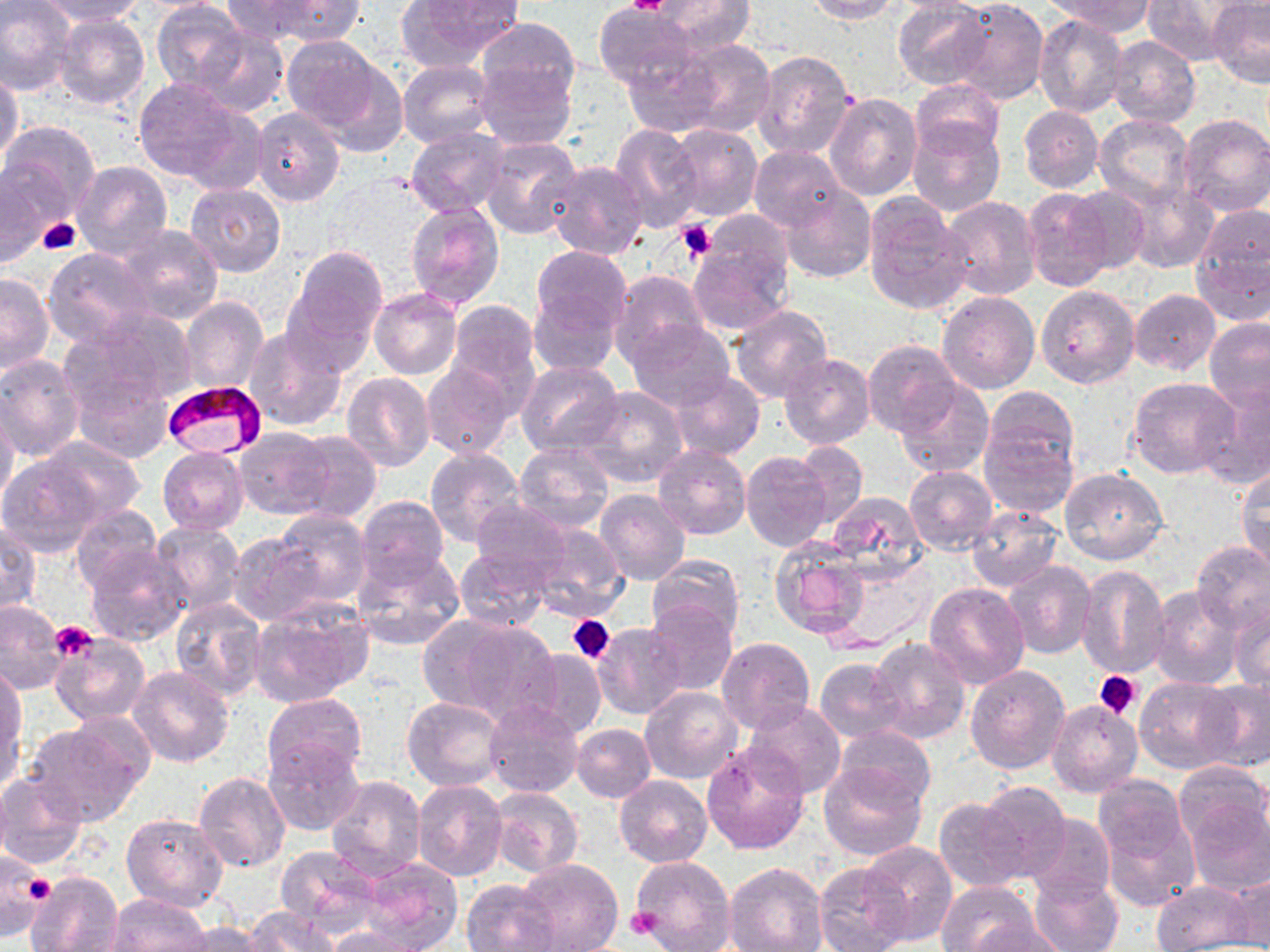

Summary:
  - Coordinate format: approximate bounding boxes as named x1/y1/x2/y2 corners in pixels
  - Plasmodium falciparum-infected red blood cell locations: (x1=162, y1=379, x2=268, y2=456)
  - Platelet locations: (x1=626, y1=0, x2=673, y2=16), (x1=38, y1=217, x2=82, y2=253), (x1=676, y1=220, x2=718, y2=262), (x1=568, y1=614, x2=615, y2=664), (x1=52, y1=624, x2=96, y2=660), (x1=1095, y1=670, x2=1141, y2=719), (x1=12, y1=866, x2=55, y2=920), (x1=626, y1=906, x2=664, y2=940)
  - Uninfected red blood cell locations: (x1=1, y1=0, x2=78, y2=96), (x1=32, y1=0, x2=148, y2=24), (x1=222, y1=0, x2=318, y2=41), (x1=254, y1=0, x2=367, y2=45), (x1=650, y1=0, x2=754, y2=56), (x1=804, y1=0, x2=899, y2=24), (x1=892, y1=0, x2=991, y2=89), (x1=949, y1=0, x2=1047, y2=105), (x1=1049, y1=0, x2=1155, y2=35), (x1=1142, y1=0, x2=1244, y2=66), (x1=1207, y1=0, x2=1270, y2=88), (x1=396, y1=1, x2=521, y2=69), (x1=152, y1=2, x2=247, y2=93), (x1=594, y1=3, x2=698, y2=93), (x1=51, y1=11, x2=150, y2=111), (x1=1034, y1=15, x2=1128, y2=118), (x1=476, y1=17, x2=582, y2=114), (x1=194, y1=27, x2=288, y2=117), (x1=281, y1=36, x2=386, y2=135), (x1=1107, y1=36, x2=1200, y2=127), (x1=679, y1=38, x2=777, y2=139), (x1=621, y1=45, x2=724, y2=136), (x1=753, y1=50, x2=857, y2=158), (x1=307, y1=51, x2=411, y2=158), (x1=476, y1=58, x2=575, y2=150), (x1=398, y1=60, x2=496, y2=149), (x1=0, y1=70, x2=22, y2=168), (x1=133, y1=76, x2=253, y2=185), (x1=912, y1=79, x2=1004, y2=158), (x1=825, y1=93, x2=922, y2=200), (x1=1018, y1=104, x2=1103, y2=194), (x1=252, y1=109, x2=344, y2=206), (x1=1178, y1=113, x2=1270, y2=218), (x1=1094, y1=114, x2=1195, y2=209), (x1=907, y1=119, x2=1004, y2=217), (x1=1, y1=120, x2=100, y2=221), (x1=668, y1=123, x2=761, y2=222), (x1=609, y1=124, x2=703, y2=233), (x1=405, y1=127, x2=510, y2=217), (x1=480, y1=135, x2=582, y2=240), (x1=748, y1=146, x2=847, y2=232), (x1=72, y1=161, x2=172, y2=260), (x1=546, y1=161, x2=648, y2=261), (x1=0, y1=163, x2=59, y2=265), (x1=185, y1=182, x2=285, y2=277), (x1=1068, y1=184, x2=1151, y2=272), (x1=1125, y1=184, x2=1218, y2=274), (x1=782, y1=186, x2=875, y2=282), (x1=1022, y1=187, x2=1114, y2=292), (x1=814, y1=193, x2=916, y2=296), (x1=863, y1=194, x2=971, y2=315), (x1=939, y1=195, x2=1041, y2=301), (x1=404, y1=201, x2=505, y2=311), (x1=1189, y1=208, x2=1269, y2=321), (x1=698, y1=212, x2=796, y2=297), (x1=113, y1=223, x2=223, y2=324), (x1=687, y1=244, x2=792, y2=336), (x1=533, y1=245, x2=631, y2=333), (x1=287, y1=246, x2=387, y2=349), (x1=43, y1=248, x2=158, y2=351), (x1=0, y1=272, x2=53, y2=376), (x1=609, y1=272, x2=710, y2=369), (x1=1036, y1=286, x2=1139, y2=389), (x1=370, y1=288, x2=462, y2=380), (x1=528, y1=288, x2=619, y2=375), (x1=1129, y1=289, x2=1220, y2=374), (x1=937, y1=291, x2=1039, y2=394), (x1=178, y1=295, x2=269, y2=396), (x1=445, y1=300, x2=541, y2=405), (x1=729, y1=305, x2=835, y2=406), (x1=77, y1=306, x2=199, y2=406), (x1=1204, y1=316, x2=1270, y2=411), (x1=629, y1=320, x2=736, y2=410), (x1=243, y1=325, x2=348, y2=431), (x1=862, y1=339, x2=962, y2=435), (x1=778, y1=352, x2=876, y2=449), (x1=0, y1=355, x2=85, y2=463), (x1=421, y1=360, x2=517, y2=462), (x1=514, y1=360, x2=622, y2=456), (x1=71, y1=369, x2=174, y2=464), (x1=342, y1=372, x2=435, y2=471), (x1=667, y1=372, x2=765, y2=459), (x1=894, y1=376, x2=994, y2=477), (x1=1127, y1=378, x2=1239, y2=479), (x1=1196, y1=382, x2=1270, y2=488), (x1=982, y1=386, x2=1079, y2=481), (x1=576, y1=387, x2=687, y2=489), (x1=0, y1=404, x2=20, y2=510), (x1=978, y1=420, x2=1077, y2=520), (x1=234, y1=427, x2=335, y2=519), (x1=289, y1=429, x2=381, y2=522), (x1=41, y1=437, x2=144, y2=521), (x1=792, y1=439, x2=868, y2=526), (x1=515, y1=443, x2=615, y2=531), (x1=653, y1=445, x2=751, y2=540), (x1=158, y1=446, x2=247, y2=534), (x1=425, y1=448, x2=524, y2=548), (x1=741, y1=451, x2=833, y2=551), (x1=0, y1=453, x2=103, y2=557), (x1=1237, y1=464, x2=1270, y2=572), (x1=904, y1=466, x2=997, y2=555), (x1=1059, y1=467, x2=1170, y2=567), (x1=594, y1=488, x2=690, y2=585), (x1=826, y1=491, x2=929, y2=583), (x1=356, y1=495, x2=451, y2=584), (x1=470, y1=497, x2=572, y2=580), (x1=965, y1=504, x2=1063, y2=592), (x1=69, y1=506, x2=163, y2=594), (x1=272, y1=510, x2=371, y2=607), (x1=526, y1=521, x2=628, y2=619), (x1=1, y1=522, x2=41, y2=615), (x1=150, y1=522, x2=245, y2=615), (x1=227, y1=533, x2=325, y2=626), (x1=768, y1=536, x2=871, y2=638), (x1=82, y1=542, x2=191, y2=647), (x1=1191, y1=542, x2=1270, y2=638), (x1=351, y1=546, x2=464, y2=652), (x1=456, y1=548, x2=551, y2=632), (x1=647, y1=554, x2=745, y2=644), (x1=1004, y1=560, x2=1097, y2=659), (x1=821, y1=562, x2=939, y2=656), (x1=1075, y1=565, x2=1170, y2=679), (x1=925, y1=582, x2=1030, y2=690), (x1=1148, y1=586, x2=1242, y2=689), (x1=1230, y1=596, x2=1269, y2=693), (x1=169, y1=597, x2=267, y2=701), (x1=1, y1=601, x2=66, y2=692), (x1=249, y1=602, x2=373, y2=704), (x1=646, y1=602, x2=738, y2=693), (x1=443, y1=619, x2=564, y2=726), (x1=593, y1=623, x2=688, y2=720), (x1=52, y1=633, x2=149, y2=725), (x1=866, y1=636, x2=970, y2=744), (x1=717, y1=638, x2=814, y2=734), (x1=520, y1=649, x2=607, y2=739), (x1=458, y1=656, x2=579, y2=771), (x1=814, y1=657, x2=909, y2=744), (x1=1, y1=662, x2=26, y2=775), (x1=965, y1=664, x2=1072, y2=774), (x1=129, y1=666, x2=235, y2=768), (x1=1134, y1=676, x2=1239, y2=773), (x1=1197, y1=677, x2=1270, y2=772), (x1=754, y1=683, x2=914, y2=791), (x1=640, y1=686, x2=743, y2=785), (x1=261, y1=692, x2=368, y2=783), (x1=402, y1=695, x2=506, y2=790), (x1=483, y1=698, x2=584, y2=799), (x1=1046, y1=700, x2=1144, y2=798), (x1=743, y1=702, x2=847, y2=798), (x1=27, y1=718, x2=148, y2=826), (x1=572, y1=724, x2=656, y2=803), (x1=833, y1=726, x2=936, y2=807), (x1=263, y1=737, x2=364, y2=836), (x1=702, y1=744, x2=808, y2=854), (x1=1173, y1=764, x2=1269, y2=846), (x1=819, y1=765, x2=928, y2=862), (x1=0, y1=770, x2=88, y2=870), (x1=194, y1=771, x2=290, y2=872), (x1=615, y1=775, x2=712, y2=867), (x1=324, y1=776, x2=426, y2=881), (x1=974, y1=779, x2=1074, y2=880), (x1=412, y1=780, x2=509, y2=881), (x1=488, y1=786, x2=583, y2=879), (x1=1093, y1=786, x2=1201, y2=914), (x1=1184, y1=795, x2=1269, y2=894), (x1=933, y1=797, x2=1030, y2=893), (x1=122, y1=812, x2=228, y2=912), (x1=1023, y1=812, x2=1115, y2=900), (x1=860, y1=842, x2=956, y2=946), (x1=275, y1=845, x2=382, y2=932), (x1=0, y1=852, x2=54, y2=939), (x1=630, y1=855, x2=737, y2=952), (x1=353, y1=858, x2=465, y2=952), (x1=514, y1=858, x2=623, y2=952), (x1=725, y1=861, x2=827, y2=952), (x1=814, y1=862, x2=910, y2=952), (x1=1226, y1=869, x2=1270, y2=950), (x1=25, y1=870, x2=123, y2=952), (x1=1028, y1=874, x2=1123, y2=952), (x1=462, y1=879, x2=561, y2=951), (x1=938, y1=880, x2=1040, y2=952), (x1=1152, y1=880, x2=1255, y2=951), (x1=105, y1=894, x2=212, y2=951), (x1=242, y1=907, x2=339, y2=952), (x1=969, y1=917, x2=1068, y2=952), (x1=176, y1=920, x2=275, y2=952), (x1=320, y1=925, x2=430, y2=951)
  - Slide-level diagnosis: Plasmodium falciparum
  - Field of view: one of a larger specimen
  - Stain: May-Grünwald-Giemsa
  - Magnification: 1000x
  - Modality: optical microscopy
  - Preparation: thin blood film
  - Image size: 1270×952 pixels